Locate and identify every blood parasite.
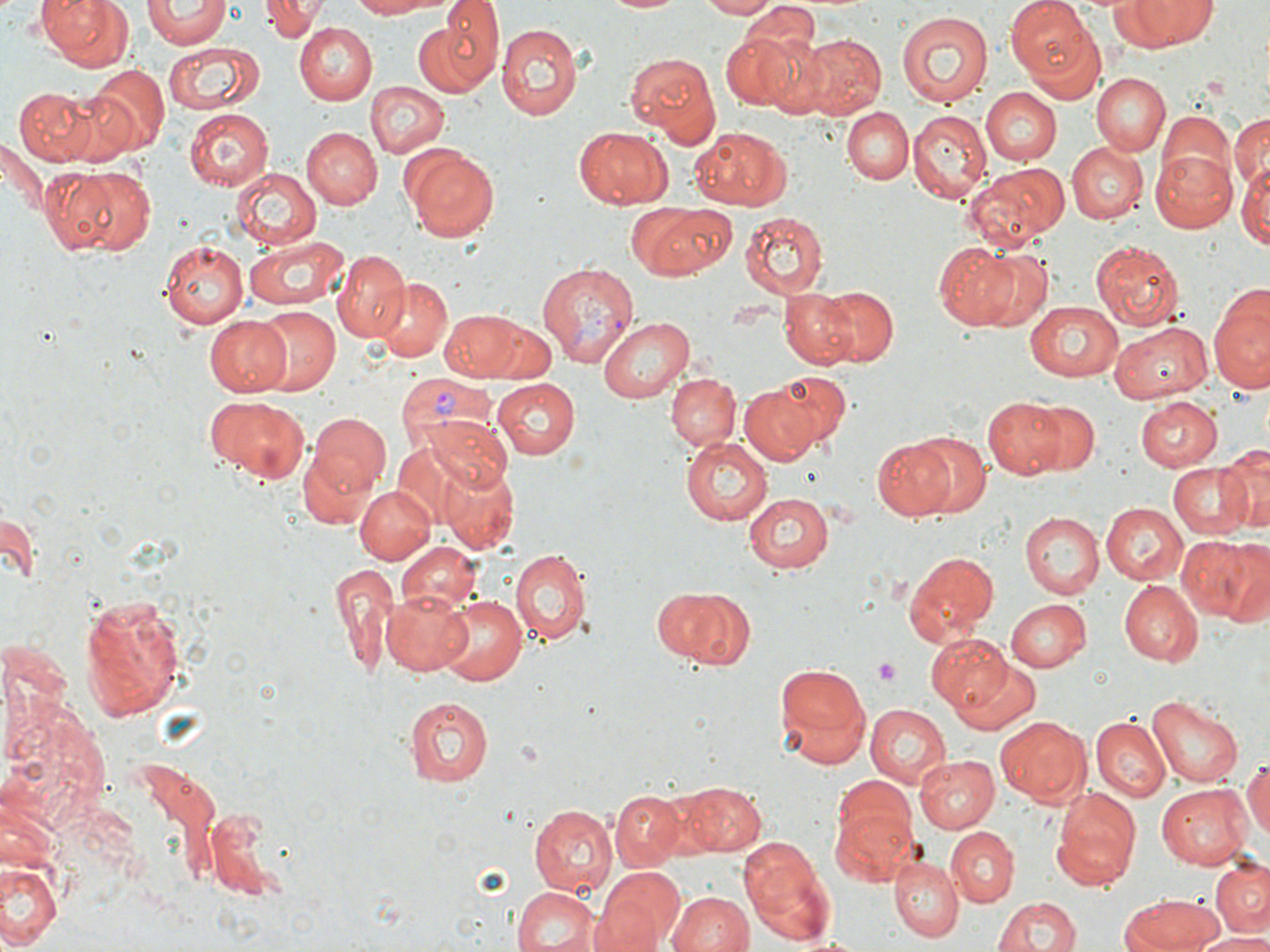
Approximate bounding boxes as (x1,y1)-(x2,y2) corner pairs in pixels.
Plasmodium vivax-infected red blood cells: (536,260)-(639,367), (396,373)-(499,461).
No Plasmodium falciparum, Plasmodium ovale, Plasmodium malariae, Babesia divergens, or Trypanosoma brucei observed.

Uninfected red blood cell locations: (43,0)-(132,72), (265,0)-(323,42), (346,0)-(441,18), (441,0)-(503,69), (599,0)-(689,15), (702,0)-(778,18), (1008,0)-(1102,87), (1123,1)-(1219,47), (144,2)-(230,48), (745,7)-(822,58), (420,10)-(502,98), (895,10)-(995,109), (498,22)-(584,120), (296,24)-(377,104), (720,31)-(804,111), (762,31)-(856,117), (799,34)-(885,118), (164,42)-(262,114), (624,50)-(722,147), (88,65)-(168,151), (1093,73)-(1168,156), (365,81)-(449,158), (12,85)-(100,165), (980,88)-(1062,165), (184,108)-(274,191), (842,108)-(913,186), (1187,109)-(1270,187), (908,110)-(991,201), (1230,111)-(1269,195), (1156,112)-(1236,198), (689,125)-(790,210), (576,126)-(673,207), (302,127)-(381,208), (0,136)-(47,221), (1066,143)-(1147,225), (404,148)-(500,243), (1152,152)-(1236,232), (1240,153)-(1270,249), (961,163)-(1071,249), (63,164)-(156,254), (231,168)-(321,250), (641,204)-(739,278), (739,212)-(829,297), (244,234)-(348,312), (935,238)-(1051,331), (160,240)-(248,329), (1089,240)-(1183,332), (334,249)-(410,342), (378,278)-(452,361), (1209,282)-(1270,394), (820,287)-(899,365), (779,288)-(857,367), (1025,300)-(1126,379), (252,307)-(340,394), (436,307)-(544,381), (204,313)-(292,395), (597,316)-(692,402), (483,320)-(555,381), (1109,322)-(1211,403), (772,370)-(852,447), (665,372)-(740,452), (491,378)-(579,458), (739,382)-(822,465), (201,395)-(308,482), (981,396)-(1068,479), (1135,397)-(1221,469), (1031,398)-(1099,476), (308,413)-(392,497), (423,417)-(513,497), (901,430)-(992,518), (680,435)-(773,525), (872,437)-(957,518), (389,438)-(499,532), (1220,440)-(1268,535), (298,441)-(377,531), (437,461)-(520,551), (1169,461)-(1250,538), (355,487)-(435,564), (744,493)-(833,573), (1101,501)-(1188,586), (1,503)-(41,587), (1021,512)-(1103,599), (1176,533)-(1263,626), (395,542)-(481,617), (507,546)-(592,647), (1217,547)-(1270,631), (900,550)-(1000,649), (328,561)-(400,676), (1118,580)-(1203,665), (657,587)-(752,669), (381,589)-(475,678), (435,594)-(526,685), (77,595)-(184,721), (1005,598)-(1090,673), (929,632)-(1020,715), (948,655)-(1040,735), (771,660)-(872,772), (1148,695)-(1245,788), (402,696)-(493,787), (865,705)-(951,788), (995,715)-(1089,803), (1089,718)-(1169,803), (1242,753)-(1270,849), (915,754)-(999,833), (831,775)-(919,859), (1155,781)-(1252,867), (681,782)-(766,857), (1051,788)-(1141,889), (610,790)-(686,869), (201,804)-(291,896), (529,804)-(616,895), (833,808)-(917,889), (943,827)-(1017,905), (740,840)-(837,944), (1,856)-(62,952), (889,856)-(962,941), (1210,858)-(1270,936), (592,866)-(686,952), (511,885)-(600,952), (666,889)-(755,950), (1120,893)-(1220,951), (993,894)-(1084,952), (1193,932)-(1270,952). Platelet locations: (872,658)-(902,684). Slide-level diagnosis: Plasmodium vivax. Light microscopy. May-Grünwald-Giemsa-stained preparation. Captured at 1000x magnification. Image is 1270×952 pixels. One field of a larger specimen. Thin blood smear.